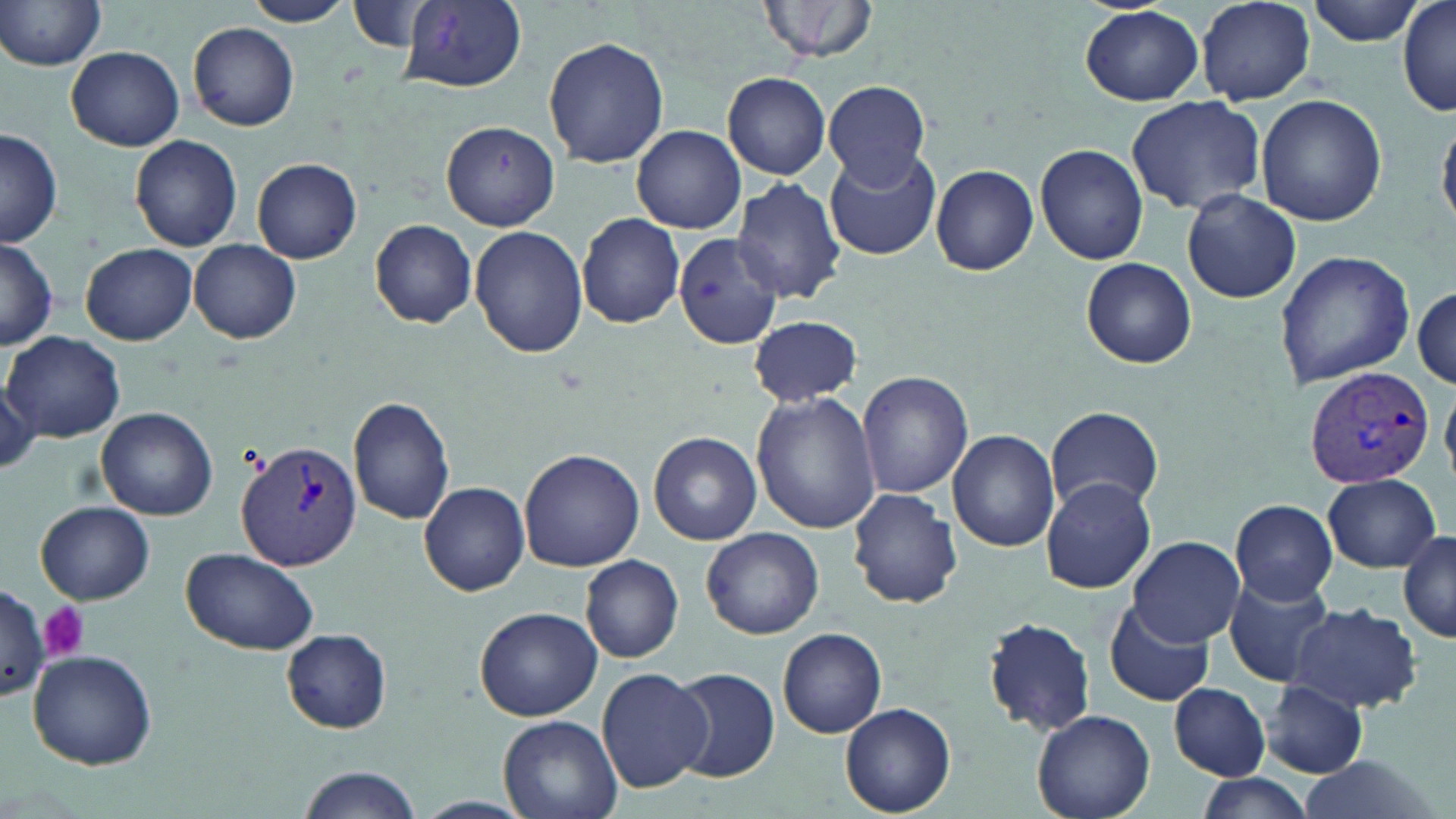

Summary:
  - Coordinate format: approximate bounding boxes as (x1,y1)-(x2,y2) corner pairs in pixels
  - Plasmodium vivax-infected red blood cell locations: (1305,364)-(1434,490), (235,441)-(366,574)
  - Platelet locations: (39,602)-(90,660)
  - Uninfected red blood cell locations: (0,0)-(107,71), (241,0)-(354,27), (759,0)-(881,64), (1195,0)-(1316,104), (1307,0)-(1426,46), (401,1)-(527,91), (348,2)-(439,54), (1396,2)-(1456,117), (1080,6)-(1203,106), (189,22)-(301,130), (544,36)-(668,169), (65,45)-(184,151), (722,72)-(831,179), (823,79)-(931,187), (1256,94)-(1386,226), (1125,96)-(1265,215), (1438,117)-(1456,232), (442,122)-(559,231), (633,125)-(744,235), (0,128)-(61,248), (131,135)-(242,252), (1035,143)-(1149,265), (826,146)-(939,259), (252,158)-(362,264), (931,164)-(1038,276), (730,177)-(846,304), (1182,189)-(1302,304), (577,212)-(686,328), (370,219)-(477,328), (471,226)-(590,359), (674,232)-(784,350), (0,238)-(58,349), (190,241)-(301,344), (81,243)-(196,345), (1273,248)-(1415,389), (1082,257)-(1197,368), (1412,285)-(1455,390), (748,314)-(861,408), (4,331)-(127,443), (0,368)-(40,475), (857,371)-(973,501), (750,390)-(880,535), (347,395)-(455,525), (1045,405)-(1165,515), (97,406)-(218,520), (949,429)-(1060,552), (648,431)-(762,545), (518,448)-(645,572), (1323,474)-(1441,572), (1040,478)-(1158,594), (420,481)-(530,596), (847,488)-(962,609), (1228,499)-(1338,605), (36,501)-(154,605), (702,526)-(823,640), (1400,528)-(1456,643), (1127,536)-(1245,647), (181,546)-(320,655), (580,555)-(684,663), (584,559)-(690,772), (1226,575)-(1339,688), (0,583)-(47,702), (1105,598)-(1215,708), (1286,603)-(1423,713), (473,606)-(603,721), (983,616)-(1098,735), (778,628)-(886,738), (281,629)-(394,733), (27,649)-(158,770), (596,667)-(712,794), (668,667)-(778,782), (1262,680)-(1370,779), (1169,683)-(1270,780), (841,702)-(957,816), (1032,708)-(1155,819), (498,713)-(623,819), (1298,756)-(1442,819), (295,767)-(420,819), (1191,774)-(1317,819), (410,796)-(535,818)
  - Slide-level diagnosis: Plasmodium vivax
  - Preparation: thin blood smear
  - Stain: May-Grünwald-Giemsa
  - Field of view: single
  - Modality: light microscopy
  - Magnification: 1000x
  - Image size: 1456×819 pixels